State which parasite is depicted.
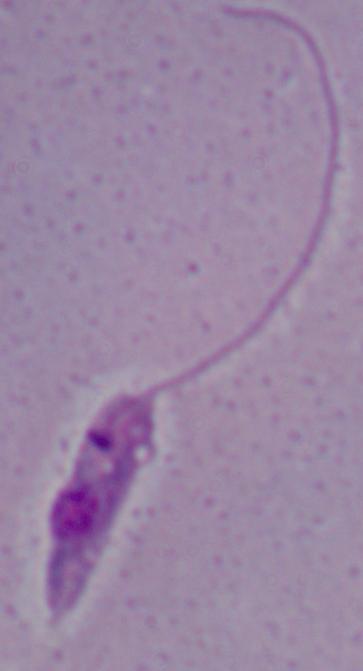

This is Leishmania.

Micrograph. 1000x magnification.